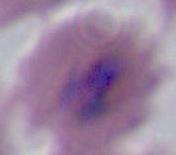
A Plasmodium parasite is shown. Photomicrograph. Captured at either 400x or 1000x magnification.